Identify the preparation type.
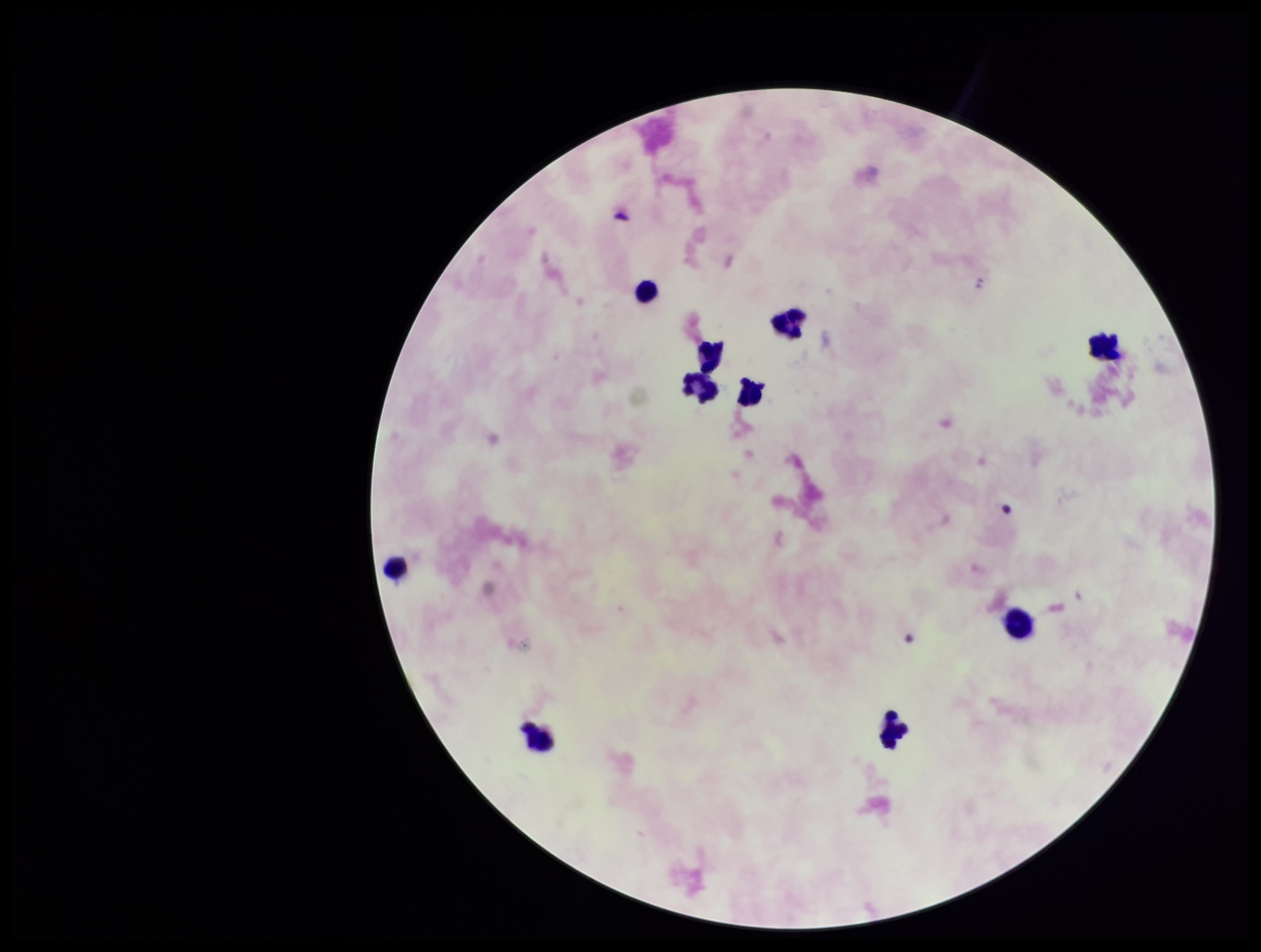
Thick.

Summary:
  - Field of view: one from this slide
  - Leukocyte count: 10
  - Capture: smartphone photograph through the microscope eyepiece
  - Parasite count: 0
  - Image size: 1261×952 pixels
  - Patient malaria status: negative
  - Plasmodium parasites: none detected
  - Stain: Giemsa